Comment on the morphology of the red blood cells.
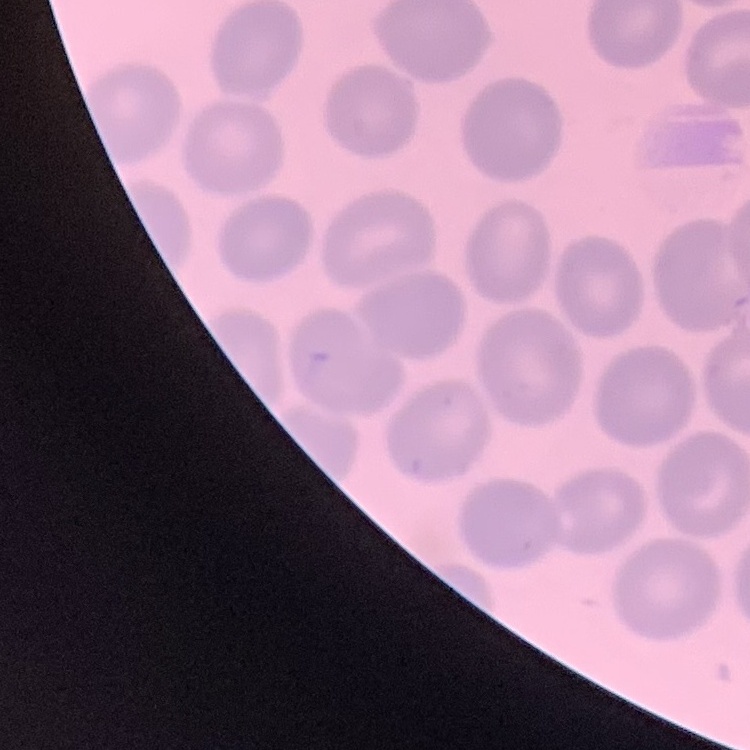

They show no rouleaux formation.

Summary:
  - Preparation: thin blood smear
  - Stain: Field's or Giemsa
  - Image type: square crop of a larger photomicrograph